Assess the morphology of the red blood cells.
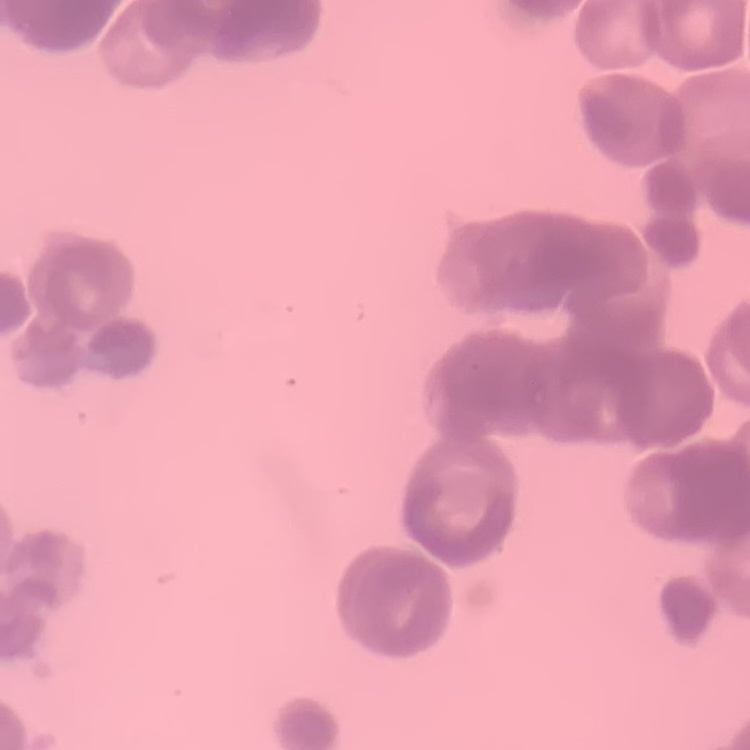

They show rouleaux formation.

One tile cut from a larger photomicrograph. Stained with either Field's or Giemsa. Thin blood film.